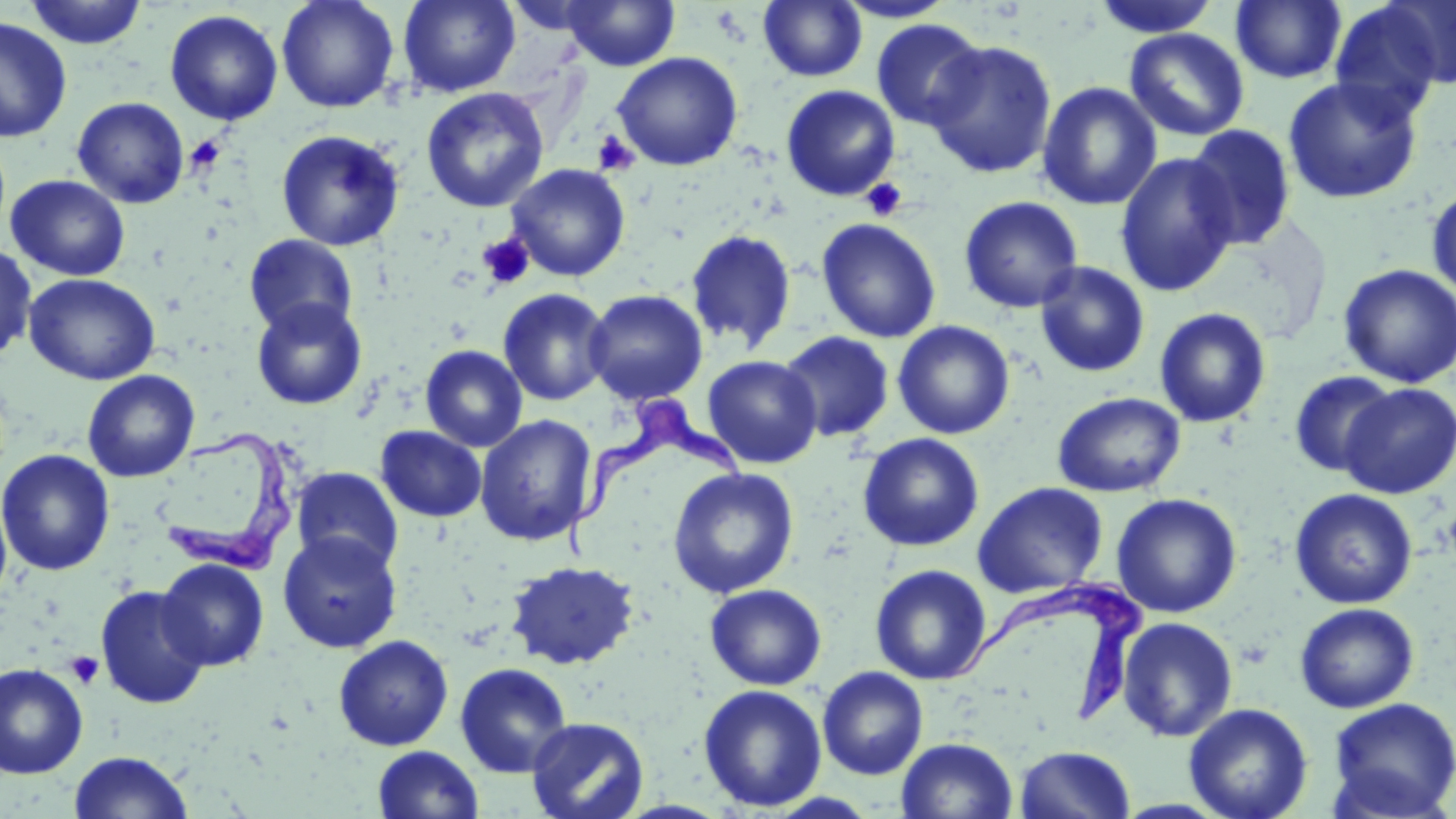
Summary:
  - Coordinate format: approximate bounding boxes as named x1/y1/x2/y2 corners in pixels
  - Platelet locations: (x1=591, y1=131, x2=640, y2=176), (x1=185, y1=134, x2=227, y2=175), (x1=860, y1=178, x2=908, y2=222), (x1=478, y1=234, x2=535, y2=289), (x1=65, y1=651, x2=104, y2=689)
  - Uninfected red blood cell locations: (x1=24, y1=0, x2=148, y2=49), (x1=277, y1=0, x2=400, y2=113), (x1=398, y1=0, x2=521, y2=97), (x1=563, y1=0, x2=680, y2=71), (x1=832, y1=0, x2=957, y2=22), (x1=1231, y1=0, x2=1346, y2=84), (x1=1380, y1=0, x2=1456, y2=89), (x1=503, y1=1, x2=609, y2=35), (x1=759, y1=1, x2=867, y2=82), (x1=1093, y1=1, x2=1221, y2=38), (x1=1328, y1=1, x2=1451, y2=122), (x1=165, y1=10, x2=283, y2=125), (x1=0, y1=17, x2=72, y2=142), (x1=870, y1=18, x2=987, y2=130), (x1=1124, y1=28, x2=1250, y2=142), (x1=926, y1=40, x2=1057, y2=178), (x1=612, y1=52, x2=743, y2=171), (x1=1282, y1=76, x2=1423, y2=204), (x1=1037, y1=82, x2=1161, y2=211), (x1=781, y1=85, x2=901, y2=201), (x1=421, y1=87, x2=548, y2=214), (x1=72, y1=96, x2=190, y2=208), (x1=1184, y1=124, x2=1296, y2=250), (x1=276, y1=130, x2=404, y2=251), (x1=1115, y1=152, x2=1238, y2=297), (x1=506, y1=163, x2=630, y2=281), (x1=6, y1=175, x2=131, y2=281), (x1=1426, y1=185, x2=1456, y2=302), (x1=958, y1=195, x2=1084, y2=313), (x1=816, y1=218, x2=941, y2=343), (x1=686, y1=230, x2=796, y2=352), (x1=243, y1=234, x2=359, y2=337), (x1=0, y1=242, x2=37, y2=361), (x1=1034, y1=261, x2=1150, y2=378), (x1=1337, y1=263, x2=1456, y2=388), (x1=24, y1=273, x2=160, y2=385), (x1=497, y1=288, x2=612, y2=406), (x1=583, y1=289, x2=708, y2=404), (x1=251, y1=298, x2=368, y2=410), (x1=1154, y1=307, x2=1271, y2=427), (x1=892, y1=320, x2=1015, y2=439), (x1=779, y1=330, x2=895, y2=442), (x1=421, y1=345, x2=527, y2=452), (x1=702, y1=355, x2=822, y2=468), (x1=82, y1=370, x2=199, y2=482), (x1=1289, y1=370, x2=1397, y2=477), (x1=1339, y1=383, x2=1456, y2=499), (x1=1053, y1=391, x2=1185, y2=497), (x1=475, y1=415, x2=597, y2=546), (x1=375, y1=426, x2=486, y2=522), (x1=858, y1=432, x2=984, y2=552), (x1=1, y1=449, x2=115, y2=576), (x1=291, y1=467, x2=404, y2=574), (x1=667, y1=467, x2=799, y2=598), (x1=972, y1=482, x2=1108, y2=598), (x1=1289, y1=488, x2=1418, y2=609), (x1=0, y1=489, x2=12, y2=608), (x1=1111, y1=493, x2=1242, y2=618), (x1=278, y1=531, x2=402, y2=653), (x1=156, y1=558, x2=269, y2=671), (x1=505, y1=560, x2=639, y2=670), (x1=870, y1=563, x2=992, y2=685), (x1=705, y1=583, x2=827, y2=690), (x1=95, y1=585, x2=211, y2=709), (x1=1295, y1=602, x2=1419, y2=713), (x1=1117, y1=616, x2=1238, y2=742), (x1=333, y1=635, x2=453, y2=751), (x1=455, y1=662, x2=572, y2=778), (x1=0, y1=663, x2=88, y2=779), (x1=817, y1=667, x2=928, y2=780), (x1=699, y1=684, x2=827, y2=812), (x1=1327, y1=697, x2=1456, y2=817), (x1=1183, y1=702, x2=1313, y2=819), (x1=526, y1=717, x2=649, y2=819), (x1=897, y1=737, x2=1018, y2=819), (x1=373, y1=745, x2=484, y2=818), (x1=1015, y1=745, x2=1136, y2=818), (x1=68, y1=750, x2=194, y2=819)
  - Trypanosoma brucei locations: (x1=563, y1=392, x2=752, y2=560), (x1=159, y1=430, x2=299, y2=575), (x1=939, y1=577, x2=1149, y2=721)
  - Slide-level diagnosis: Trypanosoma brucei
  - Preparation: thin blood film
  - Stain: May-Grünwald-Giemsa
  - Modality: optical microscopy
  - Magnification: 1000x
  - Image size: 1456×819 pixels
  - Field of view: single